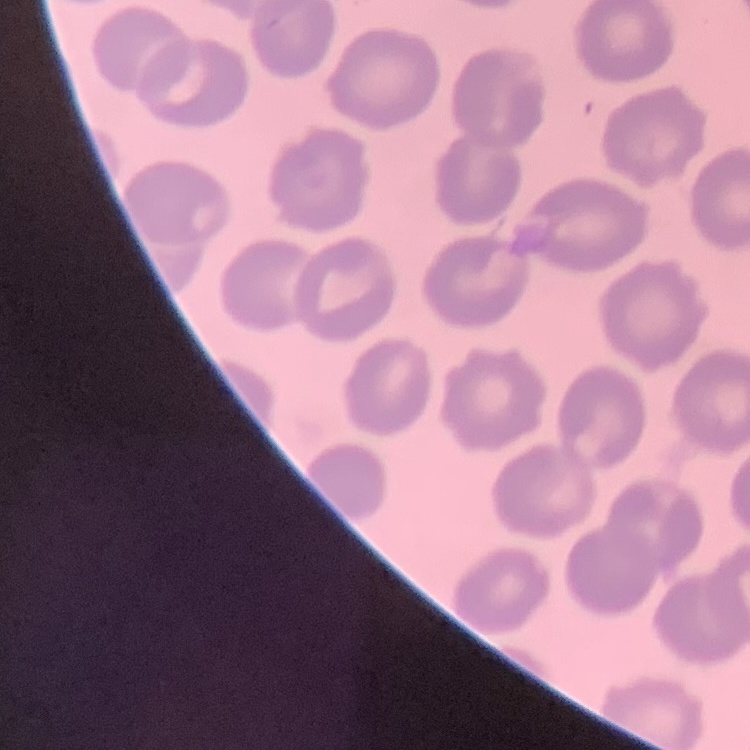
Summary:
  - Erythrocyte morphology: no rouleaux formation
  - Image type: one tile cut from a larger photomicrograph
  - Preparation: thin blood film
  - Stain: Field's or Giemsa